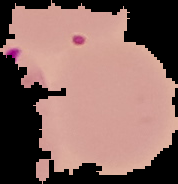
Summary:
  - Malaria status: parasitized
  - Preparation: thin blood smear
  - Image size: 178×184 pixels
  - Image type: segmented cell region on a black background